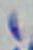

Summary:
  - Identification: Toxoplasma gondii
  - Magnification: 1000x
  - Modality: micrograph